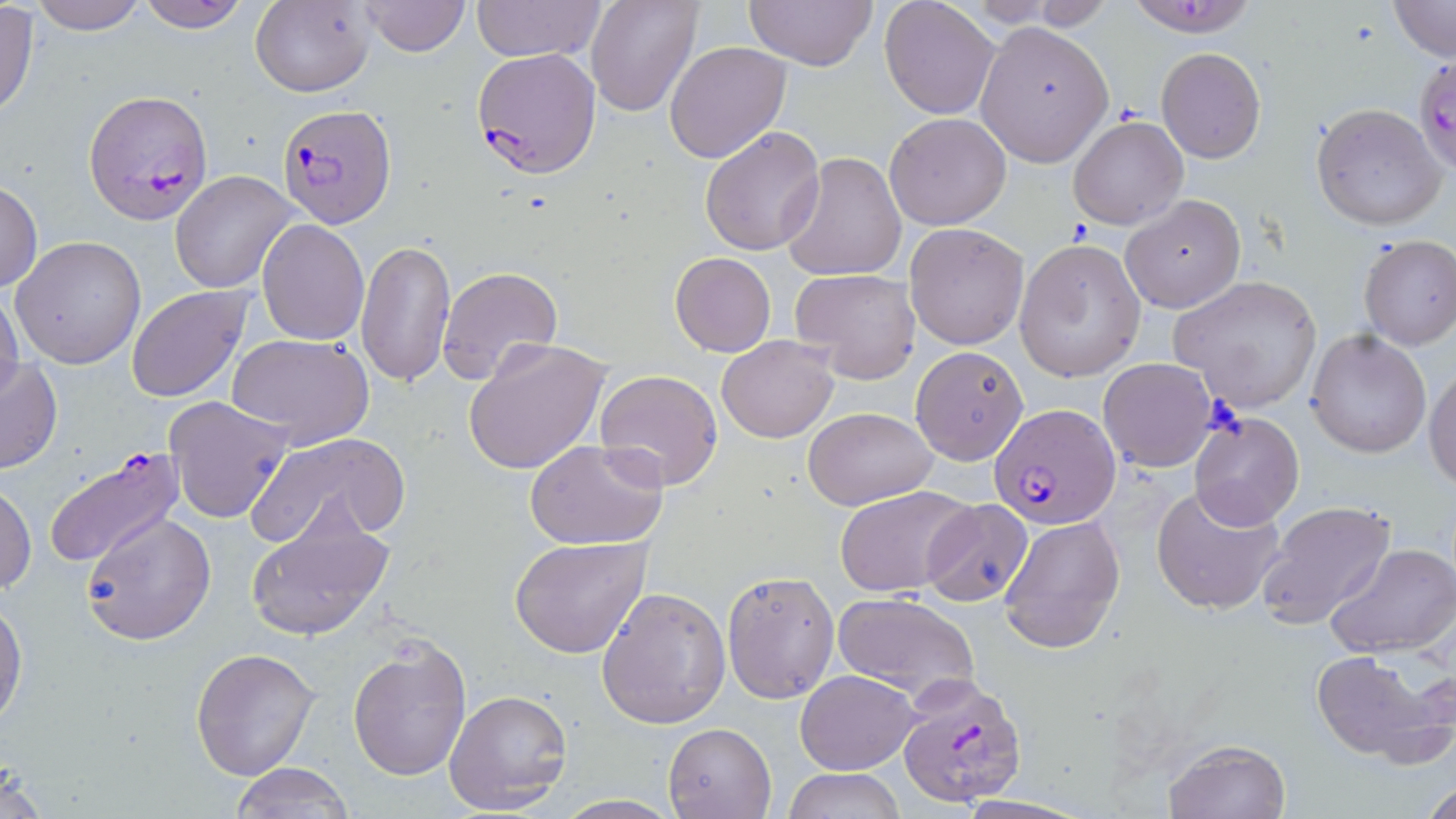
Approximate bounding boxes as (x1,y1)-(x2,y2) corner pairs in pixels. Uninfected red blood cell locations: (26,0)-(150,33), (133,0)-(254,33), (360,0)-(472,56), (471,0)-(606,64), (585,0)-(702,116), (745,0)-(878,71), (880,0)-(999,119), (249,1)-(374,96), (998,1)-(1117,30), (1388,1)-(1454,62), (0,5)-(40,120), (974,21)-(1113,166), (665,41)-(791,164), (1155,47)-(1266,162), (1311,102)-(1446,232), (885,112)-(1011,230), (1068,116)-(1188,230), (700,126)-(824,256), (782,151)-(907,282), (170,170)-(300,292), (0,178)-(42,295), (1121,194)-(1245,313), (256,219)-(370,347), (905,222)-(1029,350), (1356,235)-(1456,350), (11,236)-(146,369), (356,238)-(456,389), (1014,239)-(1146,382), (670,251)-(777,357), (438,266)-(562,385), (789,270)-(919,385), (1168,273)-(1322,413), (125,285)-(253,403), (0,287)-(24,408), (1305,330)-(1433,458), (226,334)-(374,451), (716,335)-(839,442), (460,336)-(611,476), (910,346)-(1030,464), (0,357)-(63,474), (1098,357)-(1219,472), (1426,360)-(1456,491), (594,369)-(724,492), (163,396)-(293,524), (804,406)-(938,511), (1189,413)-(1304,529), (248,431)-(411,547), (525,439)-(667,550), (1,481)-(36,596), (1151,483)-(1287,616), (834,485)-(977,597), (921,498)-(1035,605), (1256,500)-(1394,631), (244,507)-(394,642), (81,509)-(216,647), (998,515)-(1126,653), (510,535)-(654,659), (1324,542)-(1456,658), (721,570)-(840,702), (596,586)-(731,728), (831,592)-(981,703), (0,593)-(26,729), (348,636)-(471,781), (190,646)-(319,779), (1310,649)-(1452,766), (795,669)-(920,774), (444,688)-(572,815), (663,721)-(778,818), (1165,739)-(1290,818), (229,762)-(355,815), (782,767)-(907,819), (1422,777)-(1456,819), (551,794)-(683,818). Plasmodium falciparum-infected red blood cell locations: (1123,0)-(1262,38), (472,47)-(602,178), (1414,51)-(1456,181), (85,90)-(213,222), (275,104)-(397,227), (990,403)-(1121,529), (46,447)-(186,578), (897,676)-(1029,806). Slide-level diagnosis: Plasmodium falciparum. May-Grünwald-Giemsa stain. Thin blood smear. Light microscopy. 1000x magnification. One field of a larger specimen. Image is 1456×819 pixels.